State which parasite is depicted.
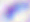
This is Toxoplasma gondii.

Photomicrograph. Captured at 400x magnification.